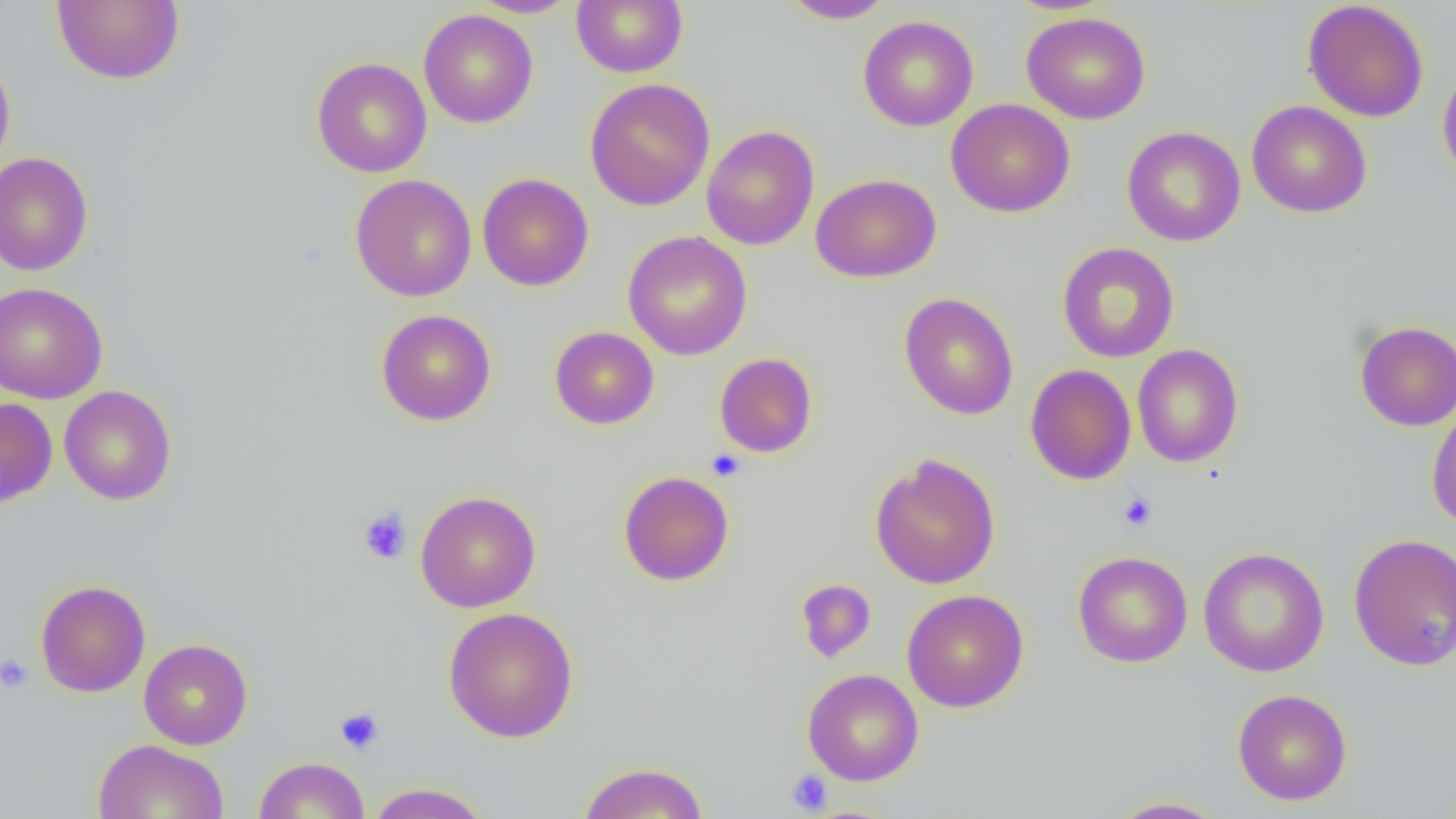
Summary:
  - Coordinate format: approximate bounding boxes as (x1,y1)-(x2,y2) corner pairs in pixels
  - Uninfected red blood cell locations: (51,0)-(185,85), (469,0)-(578,18), (571,0)-(688,77), (780,0)-(895,24), (1302,1)-(1430,123), (419,9)-(538,128), (1022,12)-(1151,125), (858,14)-(979,132), (0,48)-(16,178), (311,57)-(432,178), (1437,61)-(1456,186), (585,78)-(715,211), (946,99)-(1075,217), (1246,100)-(1372,218), (702,125)-(820,250), (1122,126)-(1246,247), (0,152)-(94,276), (478,173)-(593,291), (811,173)-(941,283), (350,174)-(477,302), (623,230)-(752,361), (1057,241)-(1179,363), (0,282)-(107,404), (898,292)-(1019,420), (376,309)-(496,425), (1354,320)-(1456,430), (549,326)-(659,429), (1132,344)-(1244,468), (714,352)-(817,458), (1025,364)-(1137,485), (59,385)-(177,505), (0,397)-(58,507), (1426,402)-(1456,531), (870,454)-(1001,590), (618,470)-(734,586), (414,491)-(541,612), (1348,533)-(1456,671), (1198,546)-(1330,677), (1072,551)-(1193,667), (35,579)-(150,697), (795,579)-(877,663), (902,589)-(1029,712), (443,606)-(579,743), (139,638)-(253,749), (802,668)-(924,786), (1232,688)-(1352,805), (93,739)-(230,819), (254,756)-(370,818), (577,761)-(710,819), (365,782)-(492,819), (1108,796)-(1231,818)
  - Platelet locations: (706,449)-(747,482), (1117,491)-(1157,532), (358,507)-(412,565), (0,654)-(34,693), (335,707)-(385,755), (786,770)-(833,815)
  - Slide-level diagnosis: negative for blood parasites
  - Image size: 1456×819 pixels
  - Modality: light microscopy
  - Preparation: thin blood smear
  - Magnification: 1000x
  - Field of view: single